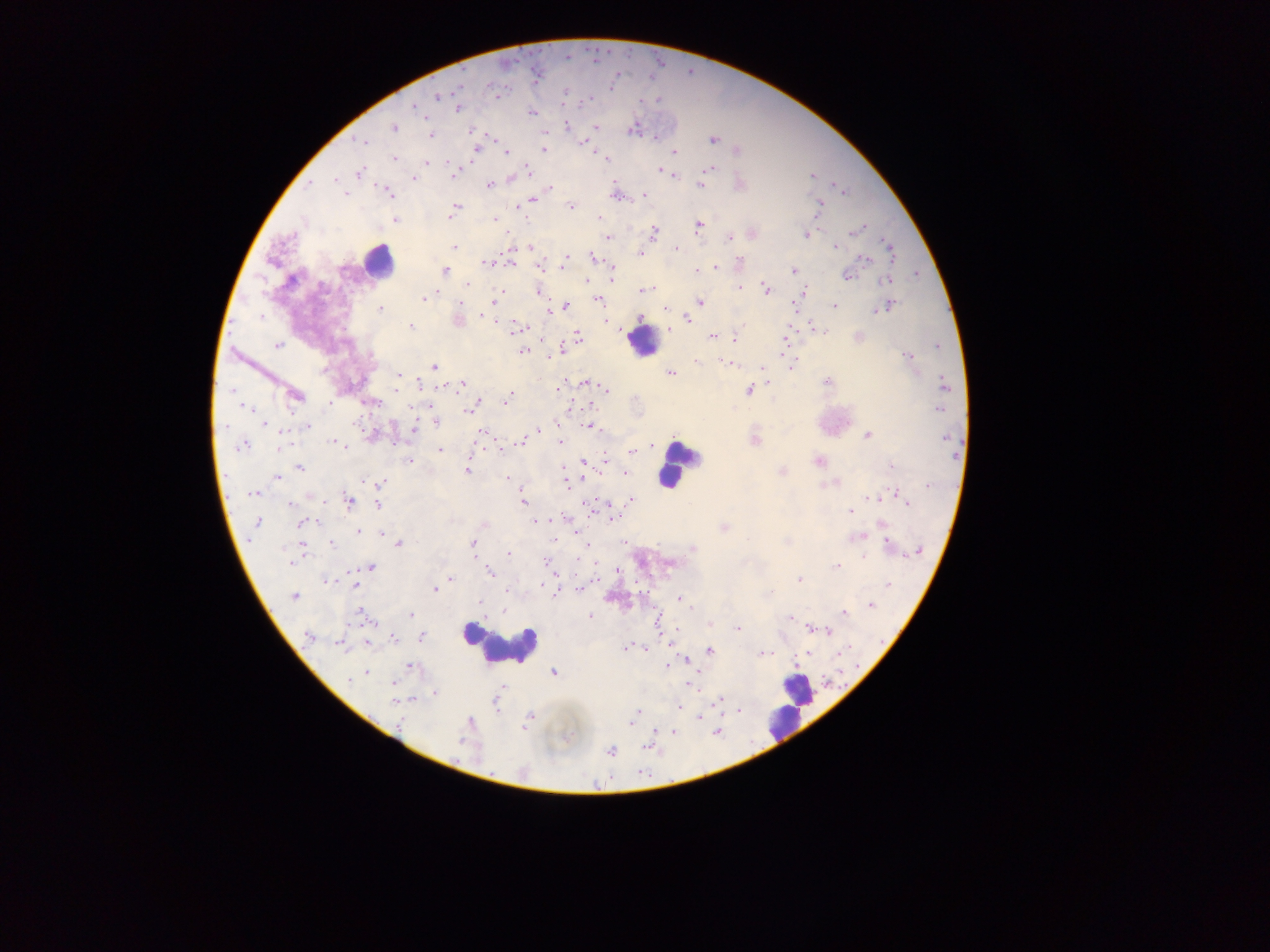
capture = mobile-phone photograph through a microscope
country = Ghana
image size = 1270×952 pixels
field of view = single
preparation = thick blood smear
leukocyte locations = approximate centers as (x, y) in pixels: (378, 261), (643, 341), (676, 465), (503, 644), (797, 692), (788, 712), (783, 726)
malaria parasite locations = approximate centers as (x, y) in pixels: (535, 78), (566, 90), (437, 96), (497, 97), (587, 99), (414, 107), (458, 108), (533, 113), (566, 125), (596, 126), (393, 127), (633, 128), (472, 131), (431, 135), (491, 137), (655, 138), (711, 139), (585, 140), (362, 141), (475, 148), (544, 149), (736, 149), (592, 151), (673, 153), (505, 154), (393, 158), (605, 159), (472, 161), (424, 162), (449, 162), (708, 168), (528, 170), (660, 171), (358, 174), (676, 175), (812, 175), (413, 178), (310, 182), (488, 184), (700, 185), (834, 185), (549, 188), (386, 190), (844, 192), (614, 194), (645, 194), (345, 195), (531, 200), (819, 205), (571, 206), (454, 208), (450, 216), (598, 218), (395, 219), (495, 219), (699, 226), (856, 230), (752, 232), (652, 233), (805, 234), (607, 237), (510, 247), (530, 247), (836, 247), (888, 247), (454, 248), (676, 249), (639, 252), (593, 256), (565, 258), (864, 258), (512, 263), (487, 264), (716, 266), (538, 267), (444, 271), (695, 271), (793, 271), (847, 275), (611, 276), (888, 280), (585, 281), (465, 284), (740, 288), (644, 289), (654, 289), (766, 289), (537, 291), (803, 293), (422, 298), (598, 300), (495, 301), (699, 302), (835, 305), (565, 306), (886, 306), (666, 307), (380, 309), (796, 311), (548, 312), (686, 317), (640, 318), (457, 320), (607, 322), (410, 327), (523, 328), (668, 329), (577, 336), (712, 336), (786, 337), (858, 337), (734, 338), (277, 345), (560, 349), (521, 351), (907, 357), (695, 361), (729, 363), (734, 363), (433, 366), (791, 366), (762, 367), (670, 372), (398, 375), (585, 382), (827, 382), (768, 383), (944, 383), (462, 384), (561, 385), (559, 390), (748, 390), (607, 391), (294, 395), (506, 399), (370, 402), (478, 402), (474, 403), (468, 406), (587, 407), (411, 408), (939, 408), (435, 419), (264, 424), (587, 425), (306, 426), (413, 429), (537, 430), (481, 431), (372, 435), (867, 435), (560, 439), (753, 440), (334, 441), (521, 442), (241, 444), (341, 444), (497, 445), (280, 447), (344, 447), (439, 449), (633, 451), (409, 460), (606, 460), (582, 461), (819, 461), (561, 465), (892, 465), (300, 467), (466, 471), (626, 472), (781, 472), (276, 477), (583, 479), (507, 480), (565, 481), (837, 482), (380, 483), (822, 484), (519, 485), (254, 493), (894, 493), (872, 497), (632, 500), (348, 501), (522, 502), (289, 503), (377, 504), (607, 504), (908, 504), (587, 505), (851, 511), (610, 518), (535, 520), (256, 522), (300, 523), (724, 527), (359, 531), (381, 532), (580, 537), (859, 537), (400, 543), (473, 543), (624, 543), (332, 544), (586, 544), (887, 544), (301, 547), (692, 549), (917, 550), (508, 553), (864, 556), (546, 560), (369, 567), (835, 567), (617, 568), (489, 572), (450, 579), (326, 580), (799, 580), (354, 584), (887, 585), (579, 589), (433, 590), (556, 591), (294, 596), (677, 598), (480, 601), (870, 605), (504, 609), (844, 613), (409, 615), (590, 615), (362, 616), (790, 617), (709, 623), (736, 629), (811, 629), (677, 630), (827, 630), (309, 636), (422, 636), (393, 638), (367, 642), (341, 643), (625, 647), (647, 648), (709, 651), (806, 653), (839, 653), (761, 654), (767, 654), (687, 661), (410, 666), (666, 666), (367, 672), (552, 672), (351, 679), (393, 684), (688, 684), (502, 686), (434, 692), (718, 699), (410, 700), (395, 701), (678, 707), (738, 710), (637, 711), (530, 717), (699, 717), (632, 724), (673, 731), (647, 745), (611, 751)